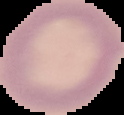
image type = segmented cell region on a black background
preparation = thin blood film
malaria status = uninfected
image size = 124×115 pixels